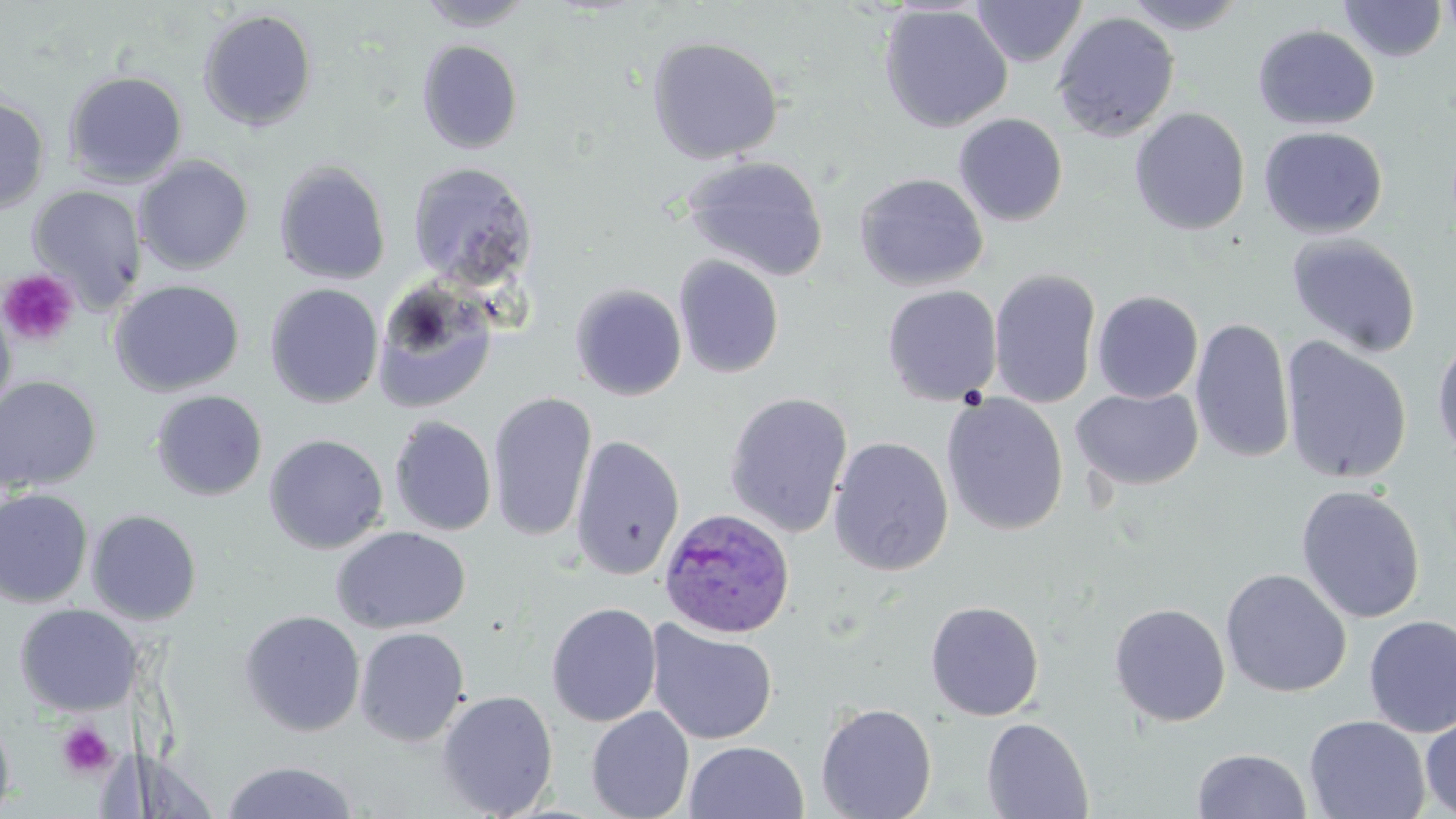

Approximate bounding boxes as [x1, y1, x2, y2] in pixels. Plasmodium ovale-infected red blood cell locations: [658, 508, 796, 638]. Platelet locations: [0, 268, 78, 349], [56, 721, 116, 779]. Uninfected red blood cell locations: [415, 0, 535, 31], [970, 0, 1087, 67], [1119, 0, 1250, 34], [1338, 0, 1449, 62], [1438, 0, 1456, 48], [878, 4, 1013, 132], [198, 9, 318, 131], [1051, 10, 1180, 142], [1253, 24, 1380, 130], [646, 35, 784, 164], [417, 39, 524, 154], [63, 69, 188, 188], [0, 95, 50, 216], [1129, 107, 1251, 235], [952, 113, 1068, 226], [1258, 126, 1388, 239], [682, 155, 830, 282], [134, 156, 254, 274], [274, 159, 391, 286], [407, 162, 538, 291], [854, 172, 989, 291], [26, 185, 148, 313], [1286, 232, 1422, 359], [674, 255, 784, 379], [988, 268, 1102, 410], [370, 278, 498, 414], [108, 279, 245, 397], [264, 283, 384, 409], [570, 283, 687, 401], [882, 285, 1003, 406], [1091, 290, 1204, 403], [0, 296, 17, 422], [1190, 317, 1296, 465], [1431, 330, 1456, 465], [1279, 336, 1413, 486], [0, 375, 102, 494], [1071, 387, 1203, 490], [150, 389, 268, 501], [488, 391, 597, 542], [724, 392, 853, 538], [941, 393, 1069, 536], [389, 415, 497, 536], [263, 433, 389, 554], [569, 434, 686, 580], [828, 436, 954, 576], [1295, 484, 1426, 624], [0, 488, 94, 608], [86, 509, 203, 625], [331, 525, 471, 634], [1220, 567, 1352, 698], [925, 600, 1045, 721], [546, 602, 662, 727], [1109, 602, 1230, 727], [14, 603, 142, 717], [239, 609, 366, 737], [1363, 614, 1456, 737], [646, 620, 778, 745], [353, 626, 470, 746], [436, 689, 559, 818], [815, 702, 937, 819], [586, 706, 695, 819], [1420, 709, 1456, 817], [0, 712, 16, 818], [1304, 714, 1430, 819], [982, 717, 1094, 819], [684, 741, 809, 819], [1192, 748, 1312, 818], [220, 760, 360, 818]. Slide-level diagnosis: Plasmodium ovale. 1000x magnification. May-Grünwald-Giemsa-stained preparation. Optical microscopy. Image is 1456×819 pixels. Thin blood smear. One field of a larger specimen.